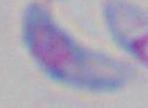
{
  "identification": "Toxoplasma gondii",
  "magnification": "1000x",
  "modality": "micrograph"
}